Classify this cell by malaria status.
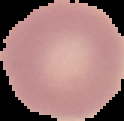
Uninfected.

image size = 124×121 pixels
image type = cell region segmented out of the field of view; surrounding area masked to black
preparation = thin blood smear